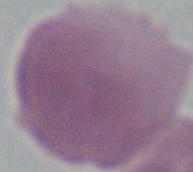

identification = erythrocyte
modality = micrograph
magnification = 1000x